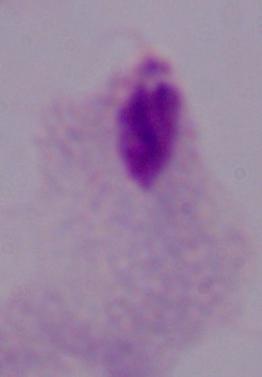

Summary:
  - Modality: micrograph
  - Magnification: 1000x
  - Identification: trichomonad